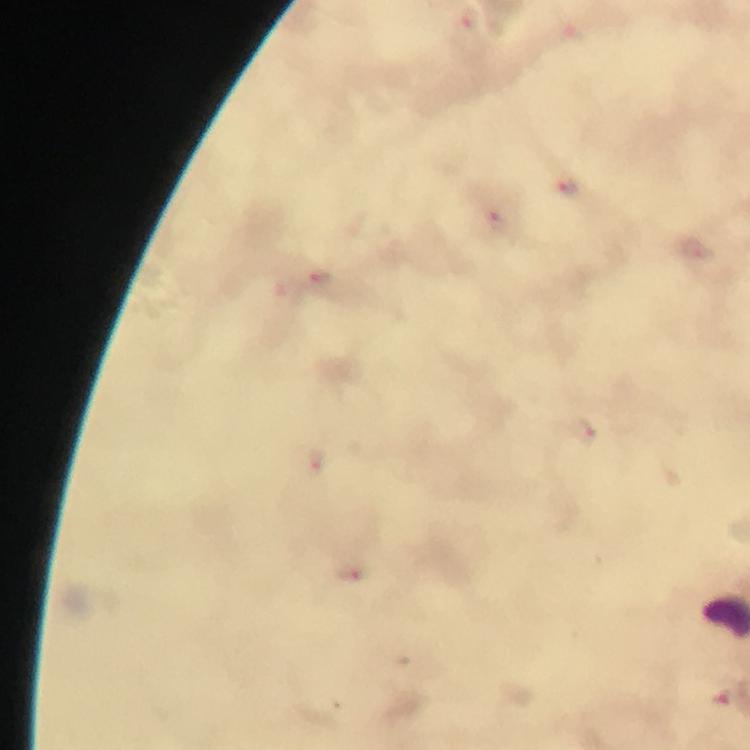
image size = 750×750 pixels
magnification = 100x
capture = smartphone mounted on the microscope
preparation = thick blood smear
Plasmodium parasite locations = approximate centers as (x, y) in pixels: (569, 186), (498, 223), (319, 277), (581, 430), (316, 459), (351, 573), (722, 695)
context = from a malaria diagnostic workup
cropped from = one field of view
immersion oil = used
stain = Giemsa